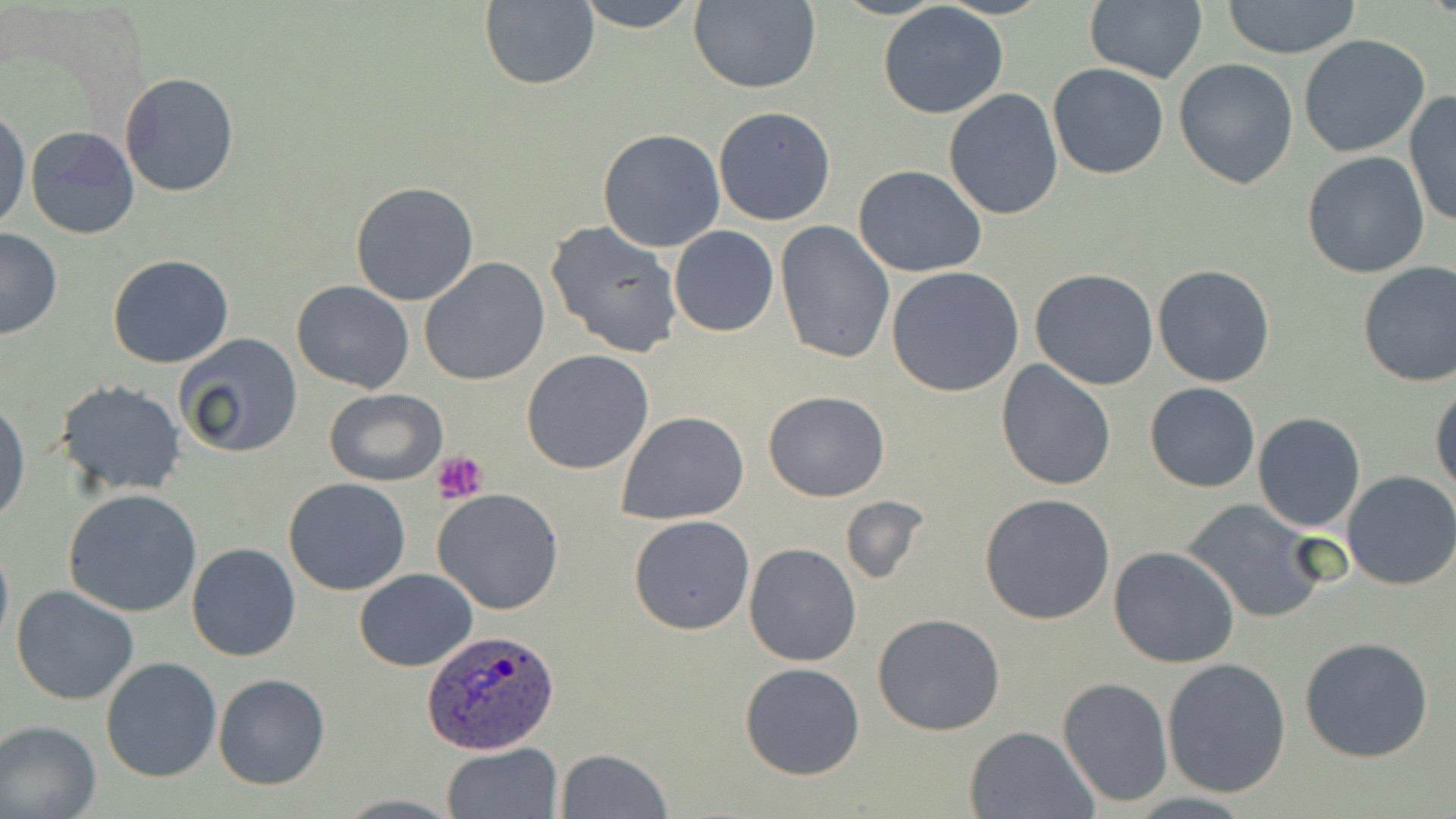

Approximate bounding boxes as [x1, y1, x2, y2] in pixels. Plasmodium ovale-infected red blood cell locations: [421, 627, 562, 755]. Platelet locations: [434, 450, 490, 503]. Uninfected red blood cell locations: [478, 0, 601, 92], [575, 0, 699, 32], [688, 0, 822, 94], [1221, 0, 1363, 58], [877, 2, 1008, 118], [1083, 2, 1207, 83], [1299, 34, 1430, 157], [1173, 58, 1298, 189], [1048, 63, 1168, 179], [119, 72, 239, 197], [943, 88, 1064, 221], [1403, 90, 1456, 230], [712, 106, 836, 226], [0, 110, 29, 231], [25, 125, 140, 240], [598, 128, 726, 252], [1302, 152, 1431, 279], [853, 164, 986, 277], [350, 180, 479, 304], [545, 220, 684, 359], [774, 220, 894, 363], [670, 226, 779, 337], [0, 228, 63, 341], [107, 253, 234, 368], [420, 259, 550, 387], [1356, 260, 1456, 386], [1153, 264, 1275, 388], [886, 266, 1026, 397], [1030, 269, 1160, 391], [291, 280, 414, 393], [174, 334, 304, 459], [522, 349, 654, 474], [996, 360, 1117, 492], [1430, 379, 1456, 497], [55, 380, 186, 497], [1145, 383, 1260, 493], [325, 389, 447, 486], [763, 390, 890, 501], [0, 400, 28, 524], [618, 412, 750, 525], [1253, 412, 1366, 533], [1342, 470, 1456, 592], [284, 477, 411, 596], [434, 488, 564, 614], [62, 489, 202, 616], [978, 494, 1116, 625], [839, 495, 928, 586], [1182, 499, 1327, 624], [628, 515, 755, 635], [0, 532, 12, 654], [186, 542, 301, 662], [743, 542, 862, 667], [1108, 546, 1240, 666], [355, 569, 476, 671], [11, 585, 139, 705], [872, 613, 1006, 736], [1299, 636, 1435, 762], [101, 656, 222, 783], [1161, 656, 1292, 797], [739, 662, 864, 780], [212, 674, 331, 790], [1058, 677, 1173, 806], [0, 720, 101, 819], [965, 725, 1097, 818], [443, 743, 564, 819], [556, 748, 672, 818]. Slide-level diagnosis: Plasmodium ovale. One field of a larger specimen. 1000x magnification. Thin blood smear. May-Grünwald-Giemsa-stained preparation. Optical microscopy. Image is 1456×819 pixels.